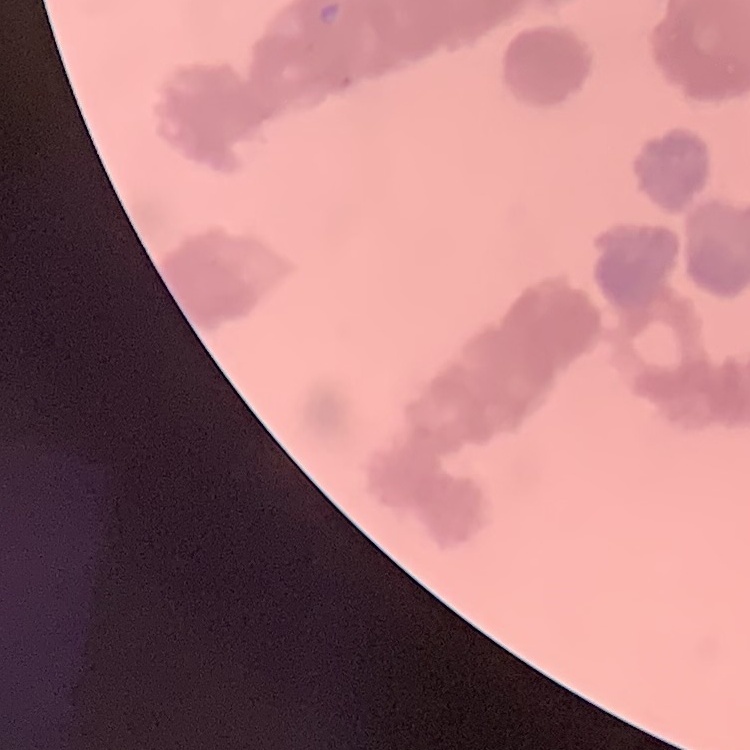

Summary:
  - Erythrocyte morphology: rouleaux formation
  - Preparation: thin blood smear
  - Stain: Field's or Giemsa
  - Image type: square crop of a larger photomicrograph